State which parasite is depicted.
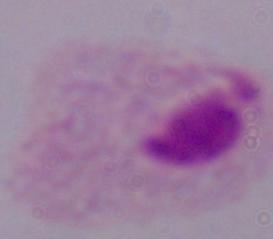
This is a trichomonad.

Photomicrograph. Captured at 1000x magnification.